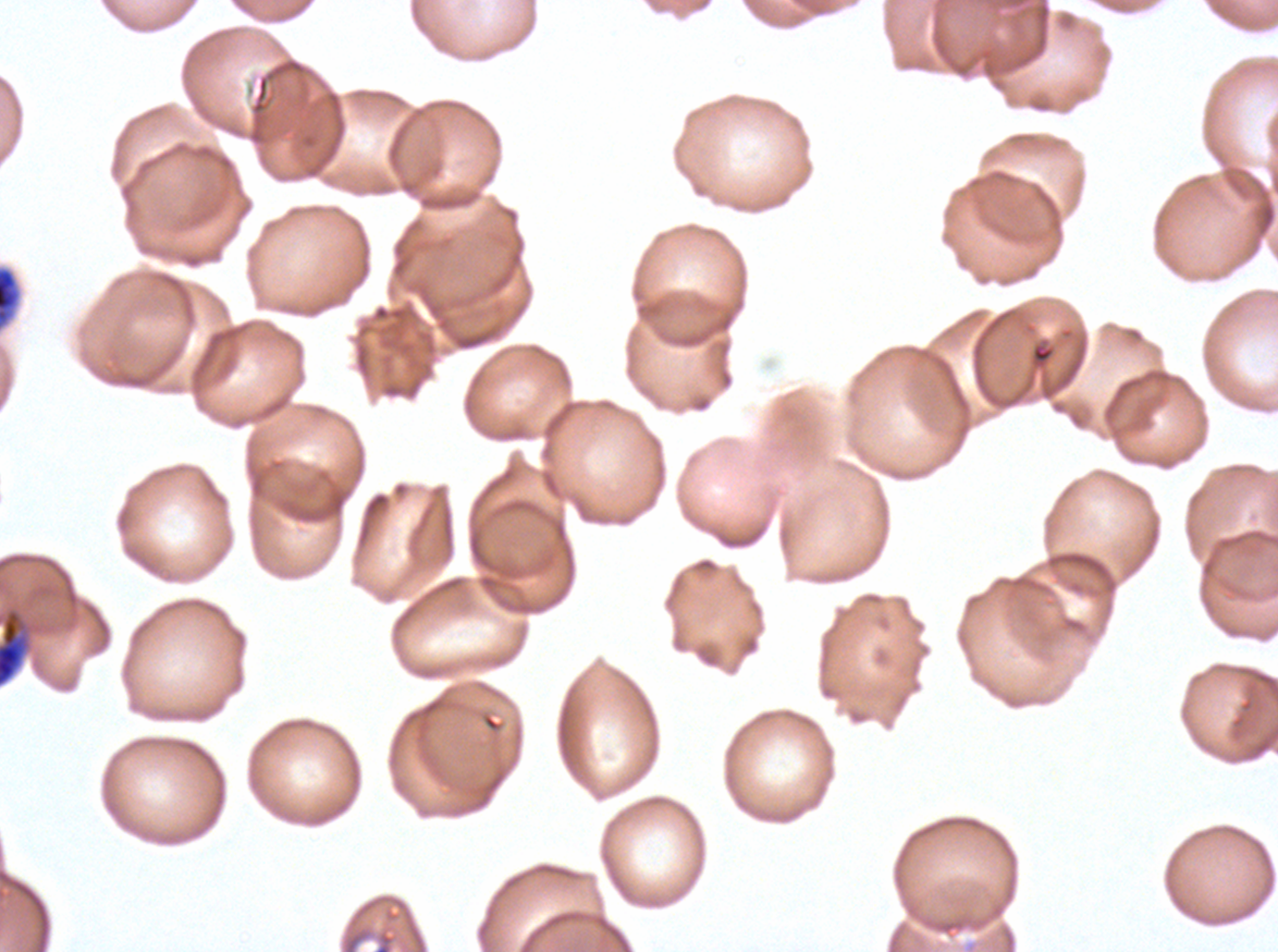
{
  "early_schizont_locations": "approximate bounding boxes as {x1, y1, x2, y2} in pixels: {0, 608, 31, 688}",
  "image_size": "1278×952 pixels",
  "preparation": "thin blood smear",
  "field_of_view": "sub-image separated from a larger composite",
  "stain": "Giemsa",
  "specimen": "Plasmodium falciparum cultured ex vivo for 24 to 48 hours, from a patient in The Gambia",
  "debris_locations": "approximate bounding boxes as {x1, y1, x2, y2} in pixels: {0, 266, 21, 330}, {339, 893, 429, 951}"
}